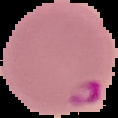

Image is 118×118 pixels. From a thin blood smear. Cell region segmented out of the field of view; the surrounding area is masked to black. Result: Plasmodium parasites identified.